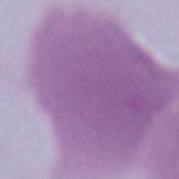

Captured at 1000x magnification. A red blood cell is seen. Micrograph.